Report the malaria status of this cell.
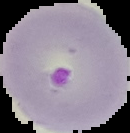
Parasitized.

From a thin blood smear. Cell region segmented out of the field of view; the surrounding area is masked to black. Image is 130×133 pixels.